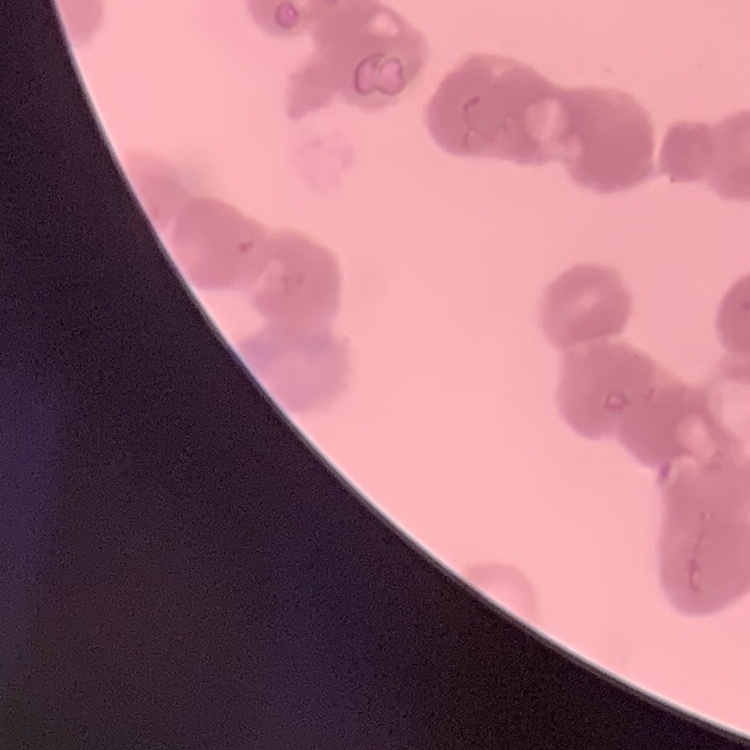
Summary:
  - Erythrocyte morphology: rouleaux formation
  - Image type: one tile cut from a larger photomicrograph
  - Stain: Field's or Giemsa
  - Preparation: thin blood film